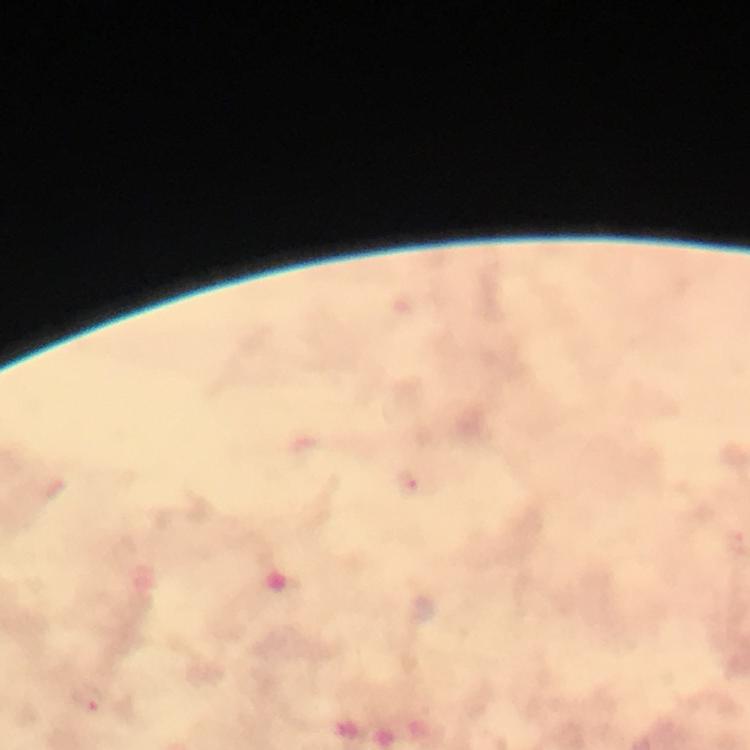
malaria parasite locations = approximate centers as {x, y} in pixels: {88, 698}
magnification = 100x
immersion oil = used
cropped from = a single field of view
stain = Giemsa
capture = smartphone photograph through a microscope
preparation = thick blood smear
image size = 750×750 pixels
context = from a diagnostic examination for malaria